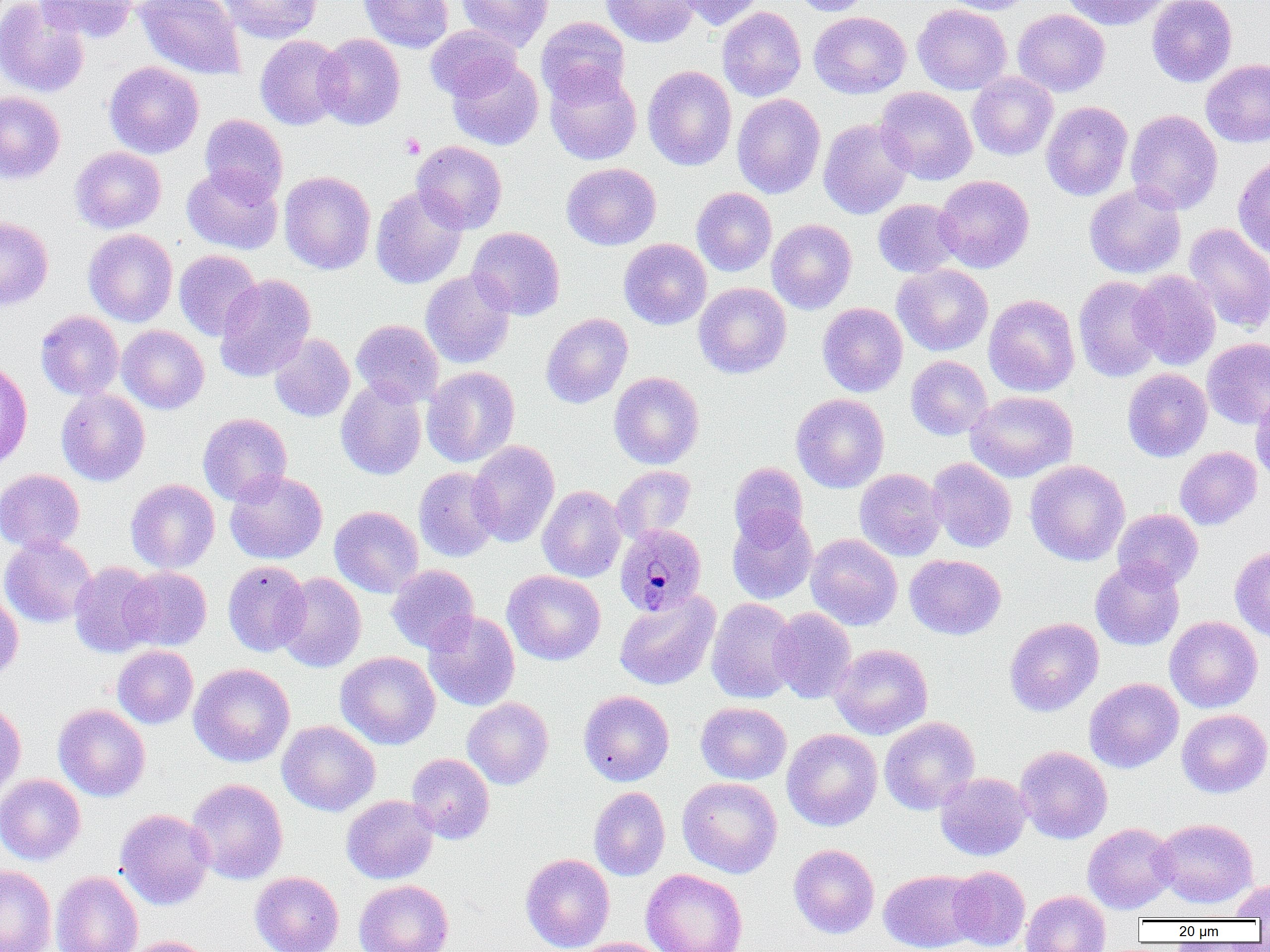
Approximate bounding boxes as (x1, y1, x2, y2) in pixels. Uninfected red blood cell locations: (0, 0, 90, 98), (136, 0, 246, 80), (217, 0, 324, 43), (359, 0, 454, 52), (456, 0, 553, 50), (601, 0, 699, 47), (678, 0, 765, 29), (790, 0, 874, 16), (941, 0, 1036, 15), (1058, 0, 1172, 30), (1147, 0, 1237, 87), (35, 1, 140, 42), (912, 3, 1011, 95), (717, 6, 806, 102), (1012, 9, 1110, 97), (808, 11, 911, 98), (536, 17, 631, 105), (426, 25, 522, 102), (315, 33, 405, 130), (255, 35, 347, 130), (1201, 58, 1270, 148), (447, 59, 543, 150), (104, 61, 204, 158), (642, 65, 737, 171), (544, 67, 642, 165), (967, 72, 1058, 161), (876, 87, 977, 185), (0, 91, 65, 184), (732, 94, 826, 198), (1041, 101, 1133, 201), (1125, 109, 1223, 214), (200, 114, 288, 203), (818, 117, 914, 219), (411, 141, 507, 234), (70, 147, 166, 234), (1233, 155, 1270, 260), (562, 162, 661, 251), (182, 164, 283, 254), (279, 171, 376, 274), (934, 175, 1035, 273), (1084, 182, 1187, 279), (370, 185, 468, 289), (691, 187, 777, 276), (873, 199, 963, 277), (0, 216, 53, 310), (767, 219, 857, 314), (1184, 223, 1270, 333), (467, 227, 565, 320), (83, 228, 178, 326), (619, 238, 711, 329), (174, 250, 261, 341), (893, 264, 994, 356), (420, 270, 516, 369), (1130, 270, 1222, 370), (214, 274, 316, 381), (1073, 275, 1167, 382), (694, 282, 791, 378), (983, 294, 1080, 396), (817, 303, 908, 397), (35, 310, 124, 400), (541, 313, 633, 408), (351, 319, 444, 407), (117, 325, 209, 414), (268, 330, 445, 414), (269, 334, 355, 422), (1202, 338, 1270, 429), (906, 355, 992, 440), (0, 360, 32, 470), (422, 367, 520, 468), (1122, 368, 1212, 462), (609, 371, 704, 469), (335, 379, 427, 480), (56, 388, 150, 486), (966, 391, 1078, 482), (1250, 392, 1270, 485), (791, 393, 889, 493), (198, 413, 292, 505), (468, 440, 560, 547), (1175, 446, 1262, 530), (927, 457, 1016, 552), (1025, 460, 1130, 565), (729, 462, 808, 546), (611, 465, 696, 541), (413, 466, 502, 562), (854, 468, 947, 561), (0, 469, 85, 553), (225, 470, 328, 564), (125, 479, 219, 573), (537, 485, 627, 583), (329, 506, 423, 597), (1112, 509, 1203, 590), (727, 510, 818, 605), (806, 533, 903, 631), (0, 535, 97, 628), (1229, 546, 1270, 642), (905, 554, 1006, 639), (1090, 559, 1185, 650), (223, 560, 311, 656), (68, 562, 161, 658), (386, 564, 479, 653), (121, 566, 212, 650), (502, 570, 606, 665), (276, 572, 366, 672), (0, 588, 24, 686), (614, 591, 720, 691), (705, 597, 800, 704), (769, 607, 857, 704), (423, 610, 520, 711), (1164, 616, 1262, 713), (1005, 617, 1104, 717), (830, 644, 933, 739), (112, 645, 198, 729), (336, 652, 440, 749), (188, 663, 295, 767), (1084, 677, 1183, 773), (578, 690, 674, 786), (462, 697, 553, 789), (0, 699, 26, 802), (695, 702, 791, 784), (53, 704, 150, 801), (1177, 708, 1269, 798), (879, 716, 980, 815), (277, 720, 380, 816), (782, 728, 882, 831), (1014, 745, 1113, 844), (406, 753, 495, 844), (935, 772, 1032, 861), (0, 774, 86, 865), (677, 777, 782, 878), (186, 778, 288, 884), (589, 786, 670, 880), (341, 795, 438, 884), (115, 808, 214, 909), (1152, 818, 1257, 908), (1082, 823, 1178, 914), (789, 844, 879, 938), (520, 853, 615, 952), (0, 864, 57, 952), (947, 865, 1030, 951), (641, 869, 748, 952), (879, 869, 981, 952), (51, 871, 143, 952), (250, 871, 344, 952), (354, 879, 453, 952), (1230, 881, 1270, 921), (1020, 890, 1110, 952), (119, 935, 215, 952), (574, 937, 670, 952). Plasmodium malariae-infected red blood cell locations: (615, 523, 707, 615). Platelet locations: (401, 134, 425, 158). Slide-level diagnosis: Plasmodium malariae. Thin blood film. Image is 1270×952 pixels. Captured at 1000x magnification. Light microscopy. Single field of view.